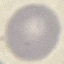
{
  "malaria_status": "uninfected",
  "capture": "smartphone camera at the microscope eyepiece",
  "image_type": "automatically extracted cell patch, resized to 64 × 64 pixels",
  "preparation": "thin blood smear",
  "stain": "Giemsa"
}